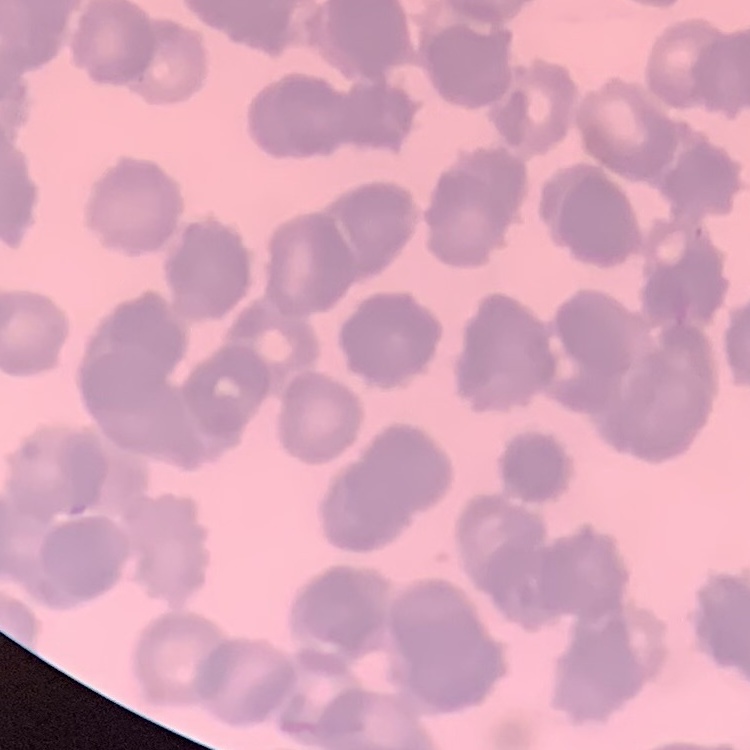
red_blood_cell_morphology: rouleaux formation
stain: Field's or Giemsa
image_type: square crop of a larger photomicrograph
preparation: thin blood smear